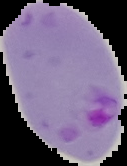

Summary:
  - Result: malaria parasites detected
  - Image size: 127×166 pixels
  - Image type: cell region segmented out of the field of view; surrounding area masked to black
  - Preparation: thin blood smear